Locate every leukocyte (white blood cell).
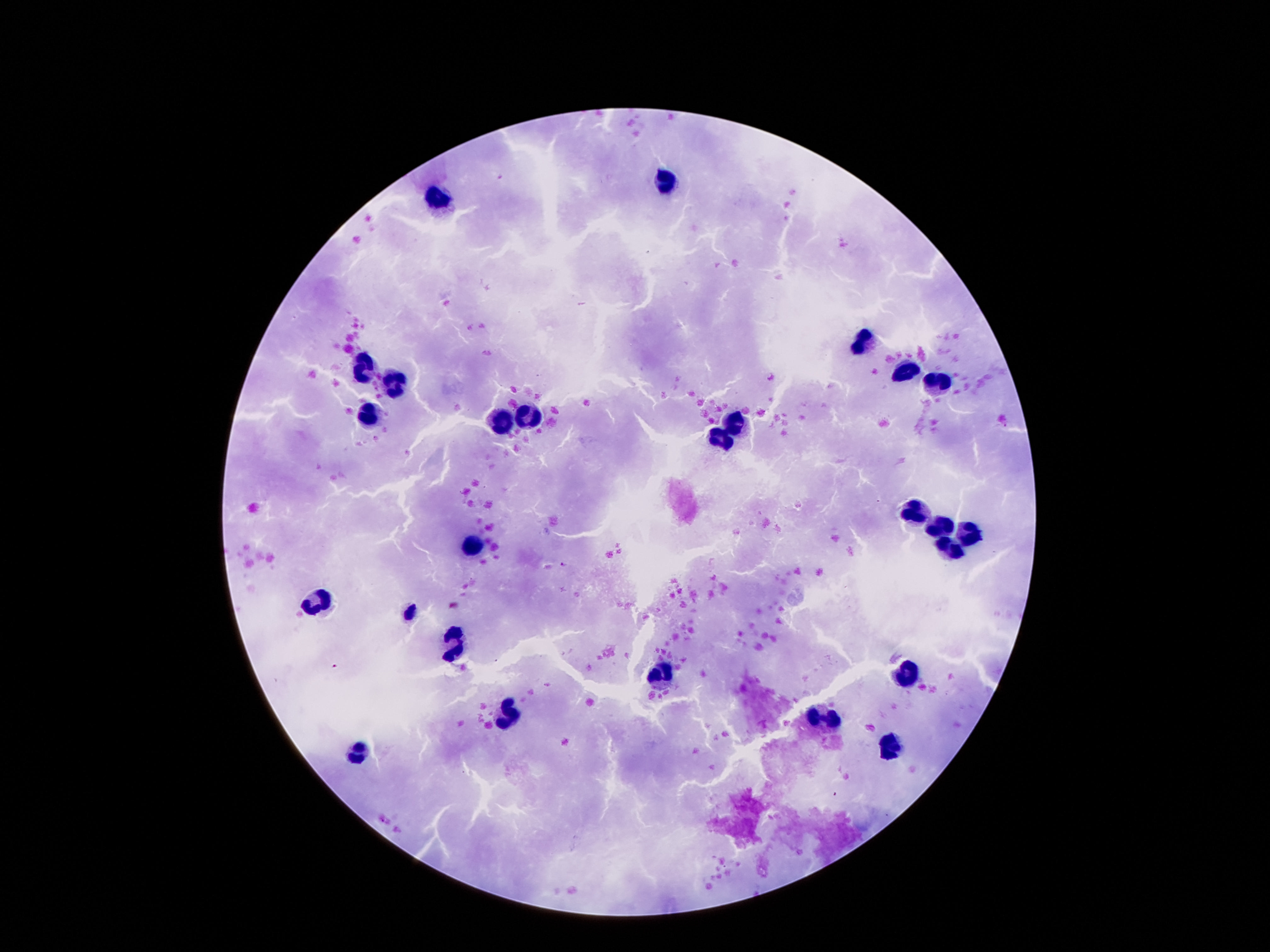
Approximate object centers, in pixels from the top-left corner.
Leukocytes: (x=665, y=181), (x=441, y=200), (x=864, y=346), (x=368, y=367), (x=903, y=369), (x=395, y=381), (x=939, y=382), (x=532, y=412), (x=369, y=416), (x=505, y=420), (x=735, y=422), (x=720, y=440), (x=917, y=513), (x=939, y=523), (x=974, y=532), (x=472, y=548), (x=946, y=550), (x=318, y=599), (x=457, y=646), (x=907, y=673), (x=660, y=675), (x=507, y=716), (x=821, y=718), (x=887, y=746), (x=360, y=755).

field of view = one from this slide
stain = Giemsa
image size = 1270×952 pixels
preparation = thick blood film
magnification = 100x
capture = smartphone camera through the microscope eyepiece
patient malaria status = uninfected